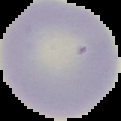
image_type: segmented cell region with the area outside set to black
image_size: 121×121 pixels
malaria_status: uninfected
preparation: thin blood smear